Name the parasite shown.
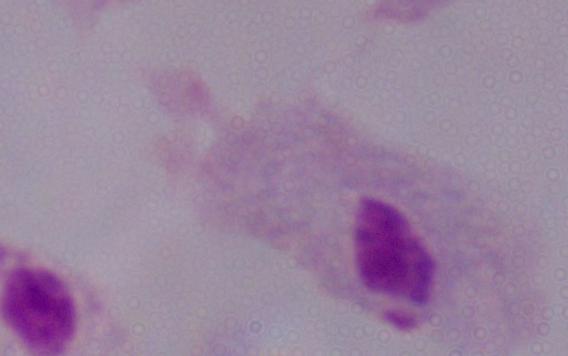

This is a trichomonad.

Captured at 1000x magnification. Photomicrograph.